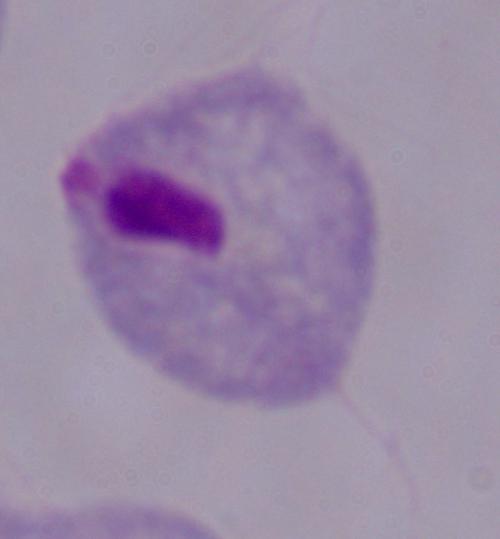
Summary:
  - Identification: trichomonad
  - Magnification: 1000x
  - Modality: micrograph